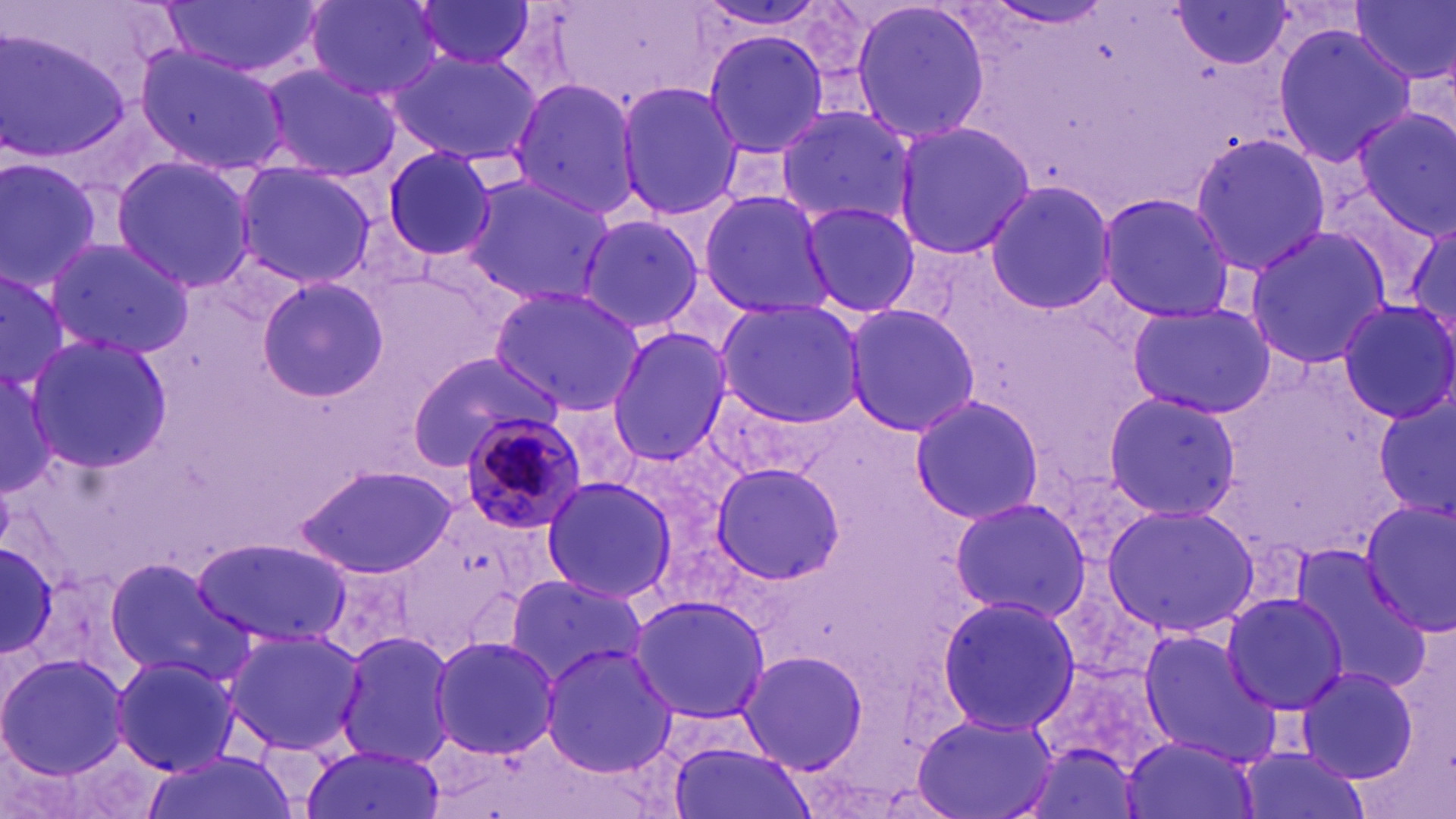

slide-level diagnosis = Plasmodium malariae
modality = light microscopy
stain = May-Grünwald-Giemsa
preparation = thin blood film
image size = 1456×819 pixels
magnification = 1000x
uninfected red blood cell locations = approximate bounding boxes as [x1, y1, x2, y2] in pixels: [304, 0, 445, 99], [848, 0, 993, 144], [410, 1, 536, 72], [1352, 1, 1455, 88], [158, 2, 320, 78], [1168, 3, 1295, 70], [1269, 22, 1418, 169], [701, 25, 833, 163], [0, 26, 128, 164], [131, 43, 292, 174], [387, 49, 544, 167], [257, 64, 404, 181], [508, 79, 640, 216], [617, 81, 743, 220], [773, 103, 917, 231], [1352, 106, 1456, 240], [889, 120, 1036, 259], [1188, 132, 1331, 278], [381, 145, 499, 263], [0, 155, 105, 291], [110, 155, 258, 291], [231, 161, 379, 286], [459, 175, 615, 308], [985, 179, 1116, 315], [698, 190, 839, 317], [1096, 192, 1239, 321], [798, 200, 920, 317], [1400, 211, 1456, 349], [576, 213, 709, 339], [1241, 227, 1395, 369], [41, 234, 194, 356], [0, 269, 77, 393], [255, 278, 390, 406], [489, 286, 645, 415], [714, 299, 866, 427], [1337, 300, 1456, 425], [1127, 301, 1277, 419], [841, 303, 983, 434], [606, 327, 733, 467], [23, 334, 172, 472], [406, 352, 560, 463], [0, 362, 61, 496], [700, 385, 854, 483], [1102, 390, 1244, 521], [908, 392, 1046, 527], [548, 400, 646, 496], [1373, 401, 1456, 515], [709, 461, 848, 589], [294, 465, 460, 578], [539, 475, 676, 605], [949, 496, 1094, 623], [1357, 499, 1456, 640], [1101, 502, 1260, 636], [0, 532, 66, 663], [191, 537, 354, 647], [1285, 543, 1433, 688], [103, 559, 249, 683], [504, 573, 648, 686], [1222, 592, 1349, 714], [934, 593, 1080, 737], [626, 595, 773, 723], [221, 626, 368, 756], [1135, 627, 1279, 767], [335, 631, 457, 766], [429, 636, 560, 758], [538, 642, 677, 779], [736, 649, 868, 772], [1029, 652, 1173, 781], [0, 653, 129, 780], [109, 653, 241, 777], [1293, 664, 1421, 784], [912, 711, 1058, 819], [1017, 732, 1150, 819], [1118, 732, 1258, 819], [668, 737, 816, 819], [1233, 745, 1372, 819], [299, 747, 447, 819], [137, 751, 298, 819]
Plasmodium malariae-infected red blood cell locations = approximate bounding boxes as [x1, y1, x2, y2] in pixels: [458, 412, 589, 534]
field of view = one of a larger specimen